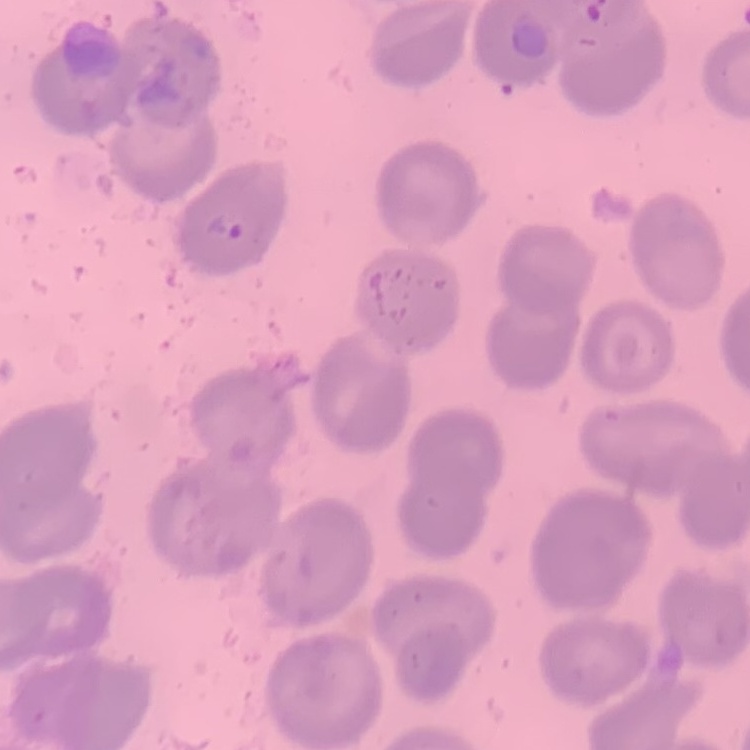

Summary:
  - Red blood cell morphology: no rouleaux formation
  - Stain: Field's or Giemsa
  - Image type: one tile cut from a larger photomicrograph
  - Preparation: thin peripheral smear